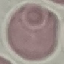
{
  "result": "no malaria parasites seen",
  "image_type": "automatically extracted cell patch, resized to 64 × 64 pixels",
  "stain": "Giemsa",
  "capture": "smartphone camera at the microscope eyepiece",
  "preparation": "thin blood smear"
}